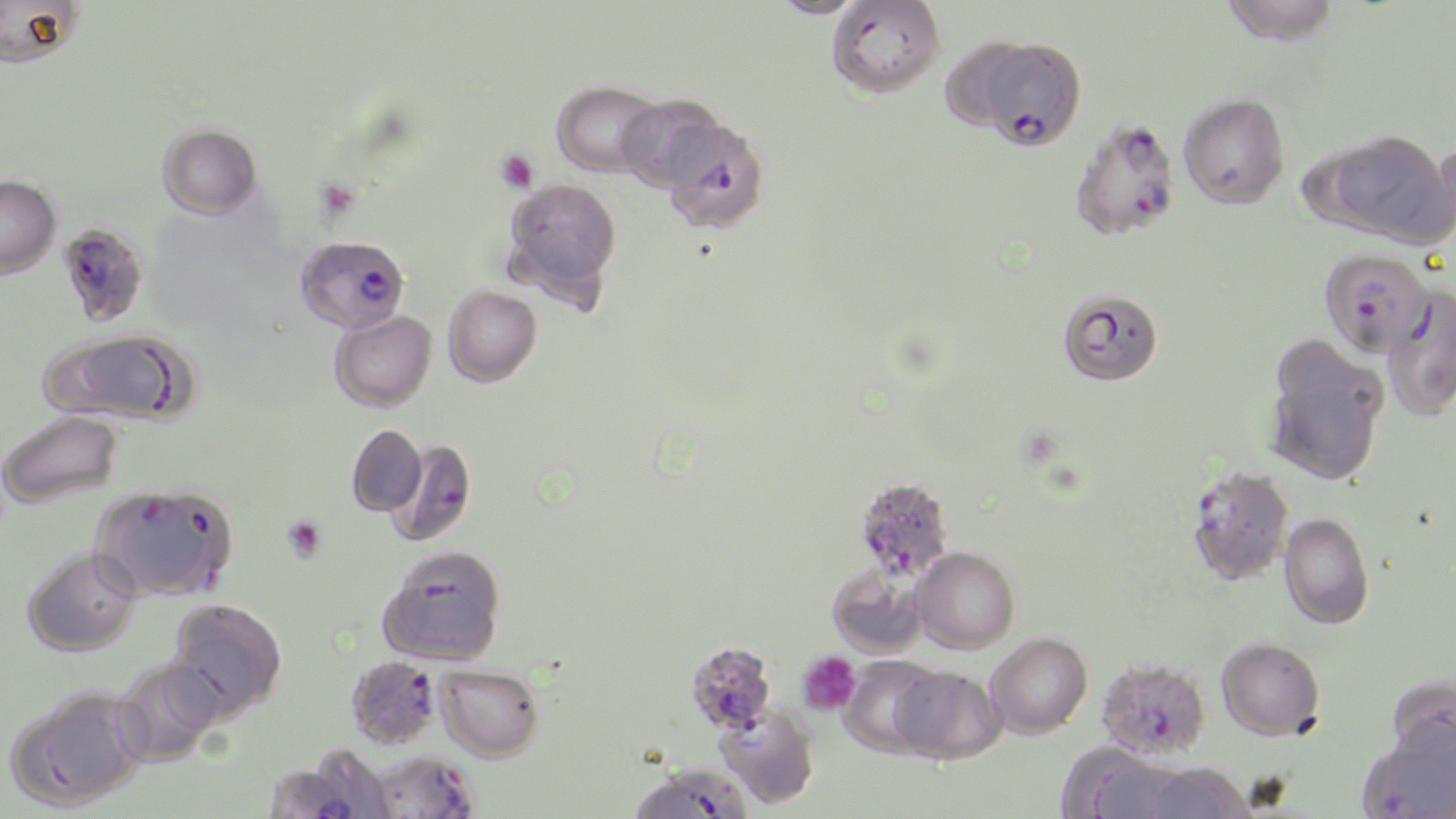
Approximate bounding boxes as (x1, y1, x2, y2) in pixels. Plasmodium falciparum-infected red blood cell locations: (982, 36, 1087, 150), (659, 118, 770, 234), (1069, 119, 1181, 242), (57, 224, 149, 326), (296, 235, 409, 333), (1320, 248, 1435, 357), (385, 436, 476, 547), (1184, 464, 1294, 585), (853, 475, 954, 581), (686, 641, 776, 734), (345, 655, 442, 749), (1097, 656, 1211, 759), (370, 749, 481, 818), (266, 764, 366, 819). Platelet locations: (495, 149, 538, 193), (282, 514, 328, 563), (796, 650, 862, 716). Uninfected red blood cell locations: (1, 0, 83, 68), (768, 0, 867, 19), (1219, 0, 1342, 45), (826, 1, 946, 99), (938, 37, 1031, 127), (552, 80, 666, 178), (1178, 92, 1290, 209), (616, 94, 729, 192), (158, 123, 262, 218), (1314, 129, 1455, 248), (1429, 132, 1456, 246), (0, 175, 60, 278), (502, 177, 623, 304), (443, 285, 542, 387), (1382, 287, 1456, 421), (1057, 289, 1164, 386), (330, 311, 437, 411), (47, 329, 197, 425), (1262, 344, 1389, 486), (0, 411, 123, 508), (346, 424, 428, 516), (91, 482, 238, 601), (1279, 512, 1374, 629), (378, 544, 507, 665), (22, 547, 141, 657), (912, 547, 1019, 653), (827, 563, 928, 658), (165, 598, 288, 721), (985, 632, 1092, 738), (1217, 635, 1326, 740), (837, 656, 944, 758), (111, 657, 224, 766), (435, 664, 544, 761), (892, 665, 1006, 763), (1385, 674, 1456, 768), (7, 686, 148, 810), (715, 704, 820, 809), (1360, 723, 1456, 819), (1058, 745, 1181, 819), (1140, 761, 1253, 819), (628, 763, 753, 819). Slide-level diagnosis: Plasmodium falciparum. Optical microscopy. Thin blood smear. May-Grünwald-Giemsa-stained preparation. 1000x magnification. Single field of view. Image is 1456×819 pixels.